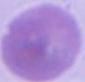

identification: erythrocyte
magnification: 1000x
modality: photomicrograph